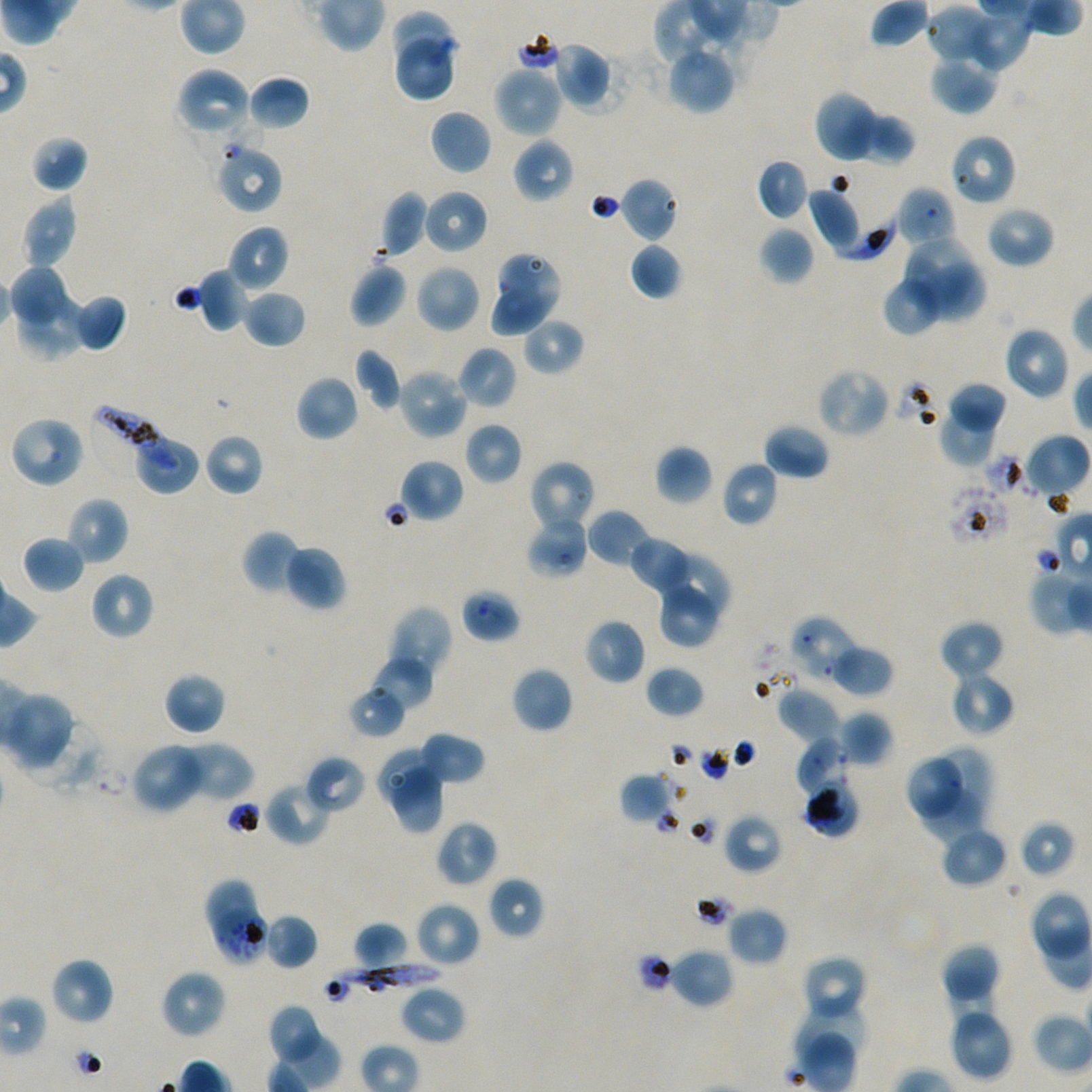
Approximate bounding boxes as [x1, y1, x2, y2] in pixels. Not every red blood cell is marked. Locations of infected red blood cells: [835, 201, 903, 261], [90, 406, 178, 475], [329, 963, 440, 999]. Locations of red blood cells of indeterminate infection status: [949, 133, 1017, 206], [215, 141, 283, 215], [460, 589, 521, 642], [790, 616, 860, 680], [806, 785, 859, 837], [204, 879, 256, 935], [216, 909, 270, 966]. Locations of uninfected red blood cells: [926, 4, 997, 67], [960, 8, 1034, 73], [392, 10, 454, 67], [397, 39, 452, 99], [551, 41, 611, 107], [665, 43, 735, 115], [930, 56, 998, 115], [493, 65, 562, 138], [175, 68, 254, 141], [247, 75, 311, 130], [814, 91, 880, 163], [429, 109, 492, 175], [856, 111, 915, 166], [29, 134, 90, 193], [512, 136, 574, 204], [755, 158, 809, 219], [620, 177, 679, 242], [895, 186, 956, 250], [808, 187, 861, 252], [423, 189, 488, 254], [380, 191, 429, 257], [22, 196, 79, 270], [985, 205, 1055, 269], [228, 225, 289, 293], [759, 227, 814, 285], [905, 239, 971, 304], [630, 242, 683, 299], [498, 253, 560, 311], [10, 260, 66, 325], [922, 260, 986, 321], [349, 263, 407, 327], [415, 264, 481, 333], [196, 268, 249, 333], [881, 276, 943, 336], [494, 287, 564, 336], [242, 289, 306, 348], [19, 291, 86, 359], [78, 291, 128, 357], [522, 316, 585, 376], [1003, 326, 1070, 400], [456, 346, 517, 410], [353, 348, 403, 411], [396, 367, 469, 440], [816, 367, 890, 438], [295, 374, 359, 441], [947, 382, 1007, 439], [937, 403, 996, 467], [9, 414, 85, 488], [464, 422, 523, 485], [763, 424, 831, 480], [204, 433, 265, 497], [1024, 434, 1090, 500], [136, 440, 197, 492], [655, 445, 713, 505], [397, 459, 464, 523], [530, 460, 596, 533], [721, 460, 780, 527], [65, 496, 129, 566], [587, 509, 652, 567], [526, 515, 589, 579], [242, 530, 303, 595], [22, 534, 86, 594], [629, 536, 694, 594], [283, 544, 347, 611], [659, 551, 731, 621], [90, 572, 154, 640], [657, 575, 723, 648], [397, 605, 453, 662], [583, 618, 645, 685], [939, 620, 1004, 682], [388, 630, 442, 680], [828, 644, 894, 695], [369, 655, 435, 711], [511, 666, 572, 733], [645, 666, 705, 718], [949, 669, 1015, 736], [163, 672, 225, 735], [347, 684, 406, 738], [776, 687, 841, 743], [1, 691, 75, 771], [837, 710, 892, 767], [416, 732, 485, 785], [795, 737, 850, 800], [130, 742, 208, 814], [177, 742, 253, 803], [928, 746, 991, 818], [377, 750, 441, 805], [304, 755, 367, 814], [909, 757, 960, 817], [390, 767, 444, 833], [619, 771, 674, 825], [265, 780, 332, 846], [920, 786, 979, 843], [722, 812, 783, 874], [1018, 819, 1076, 879], [435, 820, 498, 888], [939, 826, 1008, 888], [488, 877, 544, 939], [415, 901, 481, 967], [726, 906, 788, 966], [263, 913, 318, 970], [352, 922, 410, 969], [941, 942, 1000, 1008], [669, 948, 734, 1010], [800, 955, 867, 1022], [50, 958, 113, 1025], [160, 970, 226, 1038], [949, 978, 997, 1032], [400, 985, 466, 1044], [791, 1002, 869, 1075], [266, 1004, 326, 1066], [948, 1007, 1013, 1081]. Oil immersion, 100x objective (numerical aperture 1.45). Blood group of the donor: A+/O+. Image is 1092×1092 pixels. Giemsa stain. P. falciparum strain NF54 in static in-vitro culture. One field from this slide. Thin blood film.